Comment on the morphology of the red blood cells.
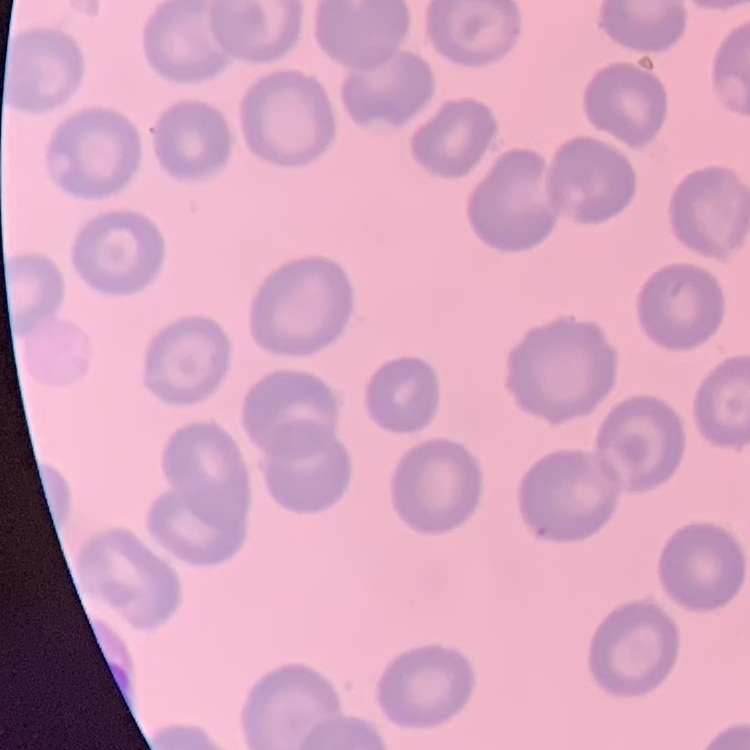
They show no rouleaux formation.

preparation = thin peripheral smear
stain = Field's or Giemsa
image type = square crop of a larger photomicrograph